Assess the morphology of the erythrocytes.
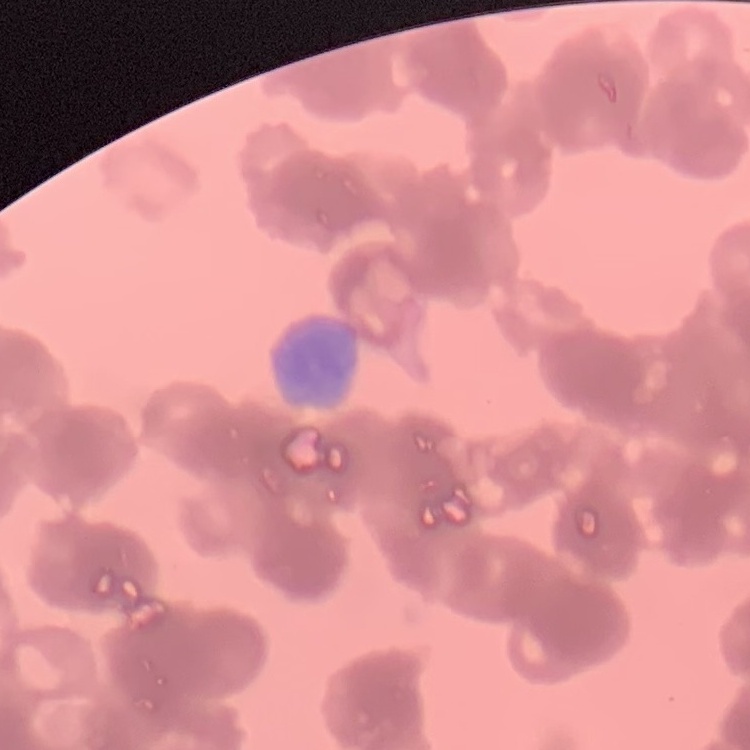

They show rouleaux formation.

Summary:
  - Stain: Field's or Giemsa
  - Image type: square crop of a larger photomicrograph
  - Preparation: thin peripheral smear